Identify the parasite.
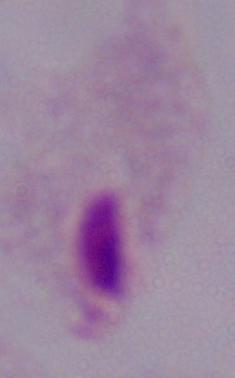

A trichomonad.

Captured at 1000x magnification. Micrograph.